Describe the morphology of the red blood cells.
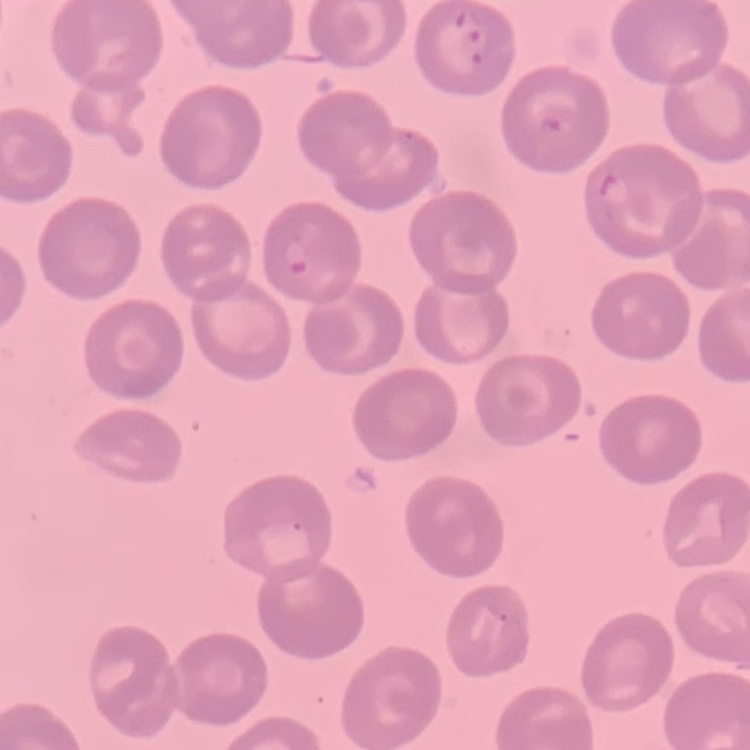

They show no rouleaux formation.

Stained with either Field's or Giemsa. One tile cut from a larger photomicrograph. Thin blood smear.